Identify the parasite.
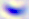
Toxoplasma gondii.

400x magnification. Micrograph.